Locate every Trypanosoma brucei.
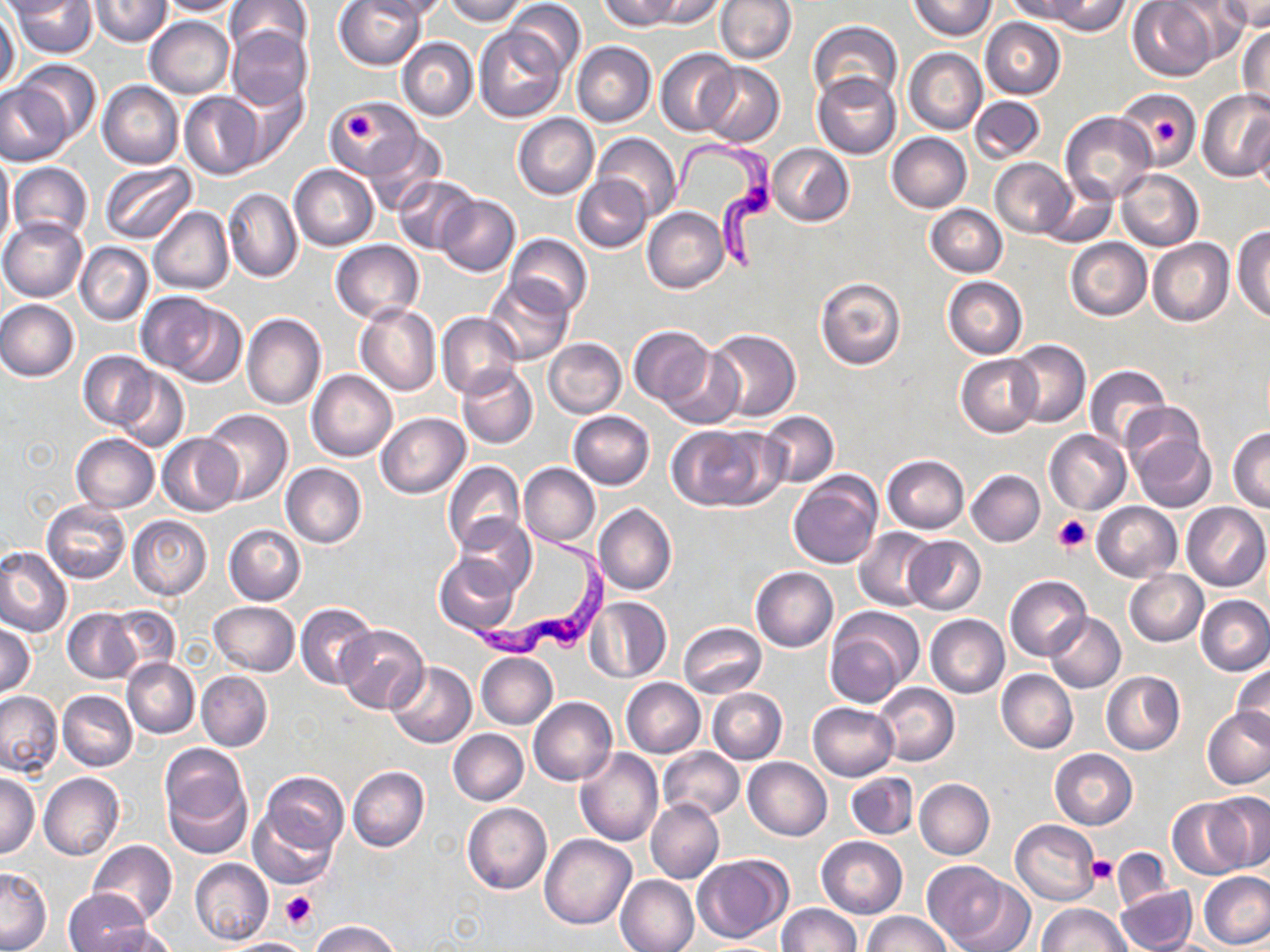

Approximate bounding boxes as [x1, y1, x2, y2] in pixels.
Trypanosoma brucei: [667, 134, 778, 273], [468, 518, 613, 659].

Platelet locations: [341, 110, 377, 143], [1152, 114, 1180, 146], [1053, 515, 1093, 553], [1087, 855, 1117, 882], [280, 891, 317, 929]. Uninfected red blood cell locations: [0, 0, 86, 18], [11, 0, 99, 57], [89, 0, 172, 46], [153, 0, 244, 15], [225, 0, 311, 64], [335, 0, 427, 70], [361, 0, 453, 20], [441, 0, 528, 25], [602, 0, 679, 30], [644, 0, 727, 29], [715, 0, 797, 65], [910, 0, 994, 40], [1002, 0, 1086, 22], [1045, 0, 1133, 36], [1128, 0, 1220, 81], [505, 1, 585, 76], [1220, 1, 1270, 31], [1166, 2, 1253, 61], [0, 7, 20, 94], [145, 16, 234, 98], [980, 17, 1066, 99], [809, 21, 901, 106], [224, 27, 311, 111], [475, 27, 565, 121], [1237, 27, 1270, 113], [397, 38, 478, 121], [572, 41, 656, 128], [904, 47, 987, 134], [655, 48, 738, 136], [15, 58, 101, 144], [699, 63, 784, 146], [813, 73, 900, 158], [98, 80, 183, 169], [0, 81, 71, 166], [231, 83, 311, 168], [1197, 89, 1270, 182], [1117, 90, 1201, 171], [180, 91, 266, 178], [970, 96, 1045, 163], [329, 101, 423, 177], [1060, 111, 1157, 205], [513, 112, 599, 200], [1253, 119, 1270, 199], [363, 132, 444, 213], [886, 132, 971, 213], [592, 133, 681, 221], [768, 143, 854, 225], [0, 149, 13, 254], [990, 157, 1076, 238], [9, 162, 92, 243], [99, 162, 196, 245], [290, 164, 378, 249], [1115, 169, 1202, 250], [392, 175, 481, 255], [572, 175, 652, 253], [1040, 179, 1118, 247], [223, 186, 303, 283], [436, 194, 520, 276], [925, 205, 1006, 277], [149, 206, 234, 295], [643, 206, 730, 294], [0, 217, 87, 301], [1232, 225, 1270, 322], [505, 234, 592, 316], [1064, 238, 1151, 321], [1148, 238, 1234, 327], [330, 240, 423, 323], [76, 241, 153, 325], [815, 275, 906, 371], [483, 276, 573, 366], [942, 276, 1027, 360], [151, 295, 246, 387], [0, 299, 79, 381], [354, 302, 440, 396], [437, 311, 523, 399], [242, 312, 325, 410], [628, 327, 713, 409], [706, 329, 801, 422], [543, 337, 626, 419], [1007, 339, 1090, 429], [661, 347, 745, 430], [77, 351, 158, 430], [957, 353, 1042, 437], [1085, 364, 1173, 452], [457, 365, 538, 449], [114, 367, 189, 453], [307, 370, 397, 461], [201, 408, 294, 505], [759, 410, 838, 488], [568, 411, 655, 489], [375, 413, 470, 498], [1126, 416, 1215, 512], [666, 422, 779, 510], [1228, 428, 1269, 513], [1044, 429, 1131, 514], [72, 433, 160, 513], [157, 433, 243, 516], [882, 455, 969, 532], [443, 461, 524, 553], [281, 463, 366, 548], [519, 463, 600, 548], [966, 470, 1044, 546], [787, 472, 883, 569], [42, 500, 131, 584], [1092, 502, 1182, 581], [1182, 502, 1269, 590], [594, 504, 677, 596], [128, 516, 213, 600], [456, 516, 534, 596], [224, 524, 306, 605], [853, 529, 939, 610], [903, 536, 986, 614], [0, 547, 72, 636], [435, 553, 521, 635], [750, 567, 838, 651], [1124, 569, 1208, 645], [1004, 575, 1091, 660], [1196, 596, 1270, 675], [584, 597, 672, 683], [210, 601, 298, 676], [296, 602, 379, 691], [104, 606, 182, 681], [64, 608, 140, 683], [825, 608, 920, 706], [1044, 612, 1126, 692], [925, 614, 1009, 698], [678, 623, 766, 698], [0, 624, 37, 697], [337, 626, 429, 714], [474, 627, 548, 655], [476, 652, 558, 729], [122, 658, 199, 738], [386, 661, 477, 747], [1232, 662, 1270, 748], [997, 669, 1077, 753], [195, 670, 272, 751], [1101, 671, 1185, 754], [622, 679, 704, 757], [874, 683, 959, 765], [709, 688, 786, 764], [0, 690, 63, 776], [59, 690, 136, 772], [530, 696, 617, 786], [808, 702, 898, 780], [1203, 707, 1270, 789], [448, 729, 528, 805], [159, 744, 251, 857], [658, 747, 744, 820], [575, 748, 664, 846], [1049, 749, 1137, 830], [743, 757, 832, 840], [348, 766, 429, 852], [39, 772, 124, 861], [259, 772, 347, 859], [847, 772, 917, 839], [1, 773, 39, 859], [915, 779, 994, 859], [1203, 792, 1270, 874], [1168, 798, 1253, 879], [646, 799, 725, 884], [462, 803, 551, 894], [250, 806, 340, 889], [1010, 819, 1099, 904], [540, 835, 636, 929], [817, 836, 907, 918], [88, 840, 177, 926], [692, 854, 790, 944], [190, 858, 274, 946], [926, 861, 1032, 951], [0, 867, 52, 951], [1198, 872, 1270, 950], [616, 875, 700, 952], [1115, 884, 1196, 952], [64, 889, 148, 950], [1037, 903, 1130, 952], [775, 904, 861, 952], [862, 910, 952, 952], [309, 921, 402, 952], [91, 924, 178, 952], [218, 938, 315, 951]. Slide-level diagnosis: Trypanosoma brucei. One field of a larger specimen. Optical microscopy. Captured at 1000x magnification. Thin blood smear. Image is 1270×952 pixels. May-Grünwald-Giemsa-stained preparation.